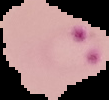
Summary:
  - Image type: segmented cell region on a black background
  - Malaria status: parasitized
  - Preparation: thin blood smear
  - Image size: 109×100 pixels